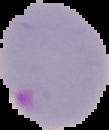 Image is 109×130 pixels. Segmented cell region on a black background. From a thin blood smear. Malaria status: parasitized.